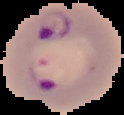

image_type: cell region segmented out of the field of view; surrounding area masked to black
image_size: 124×115 pixels
result: malaria parasites identified
preparation: thin blood film